State the blood parasite species.
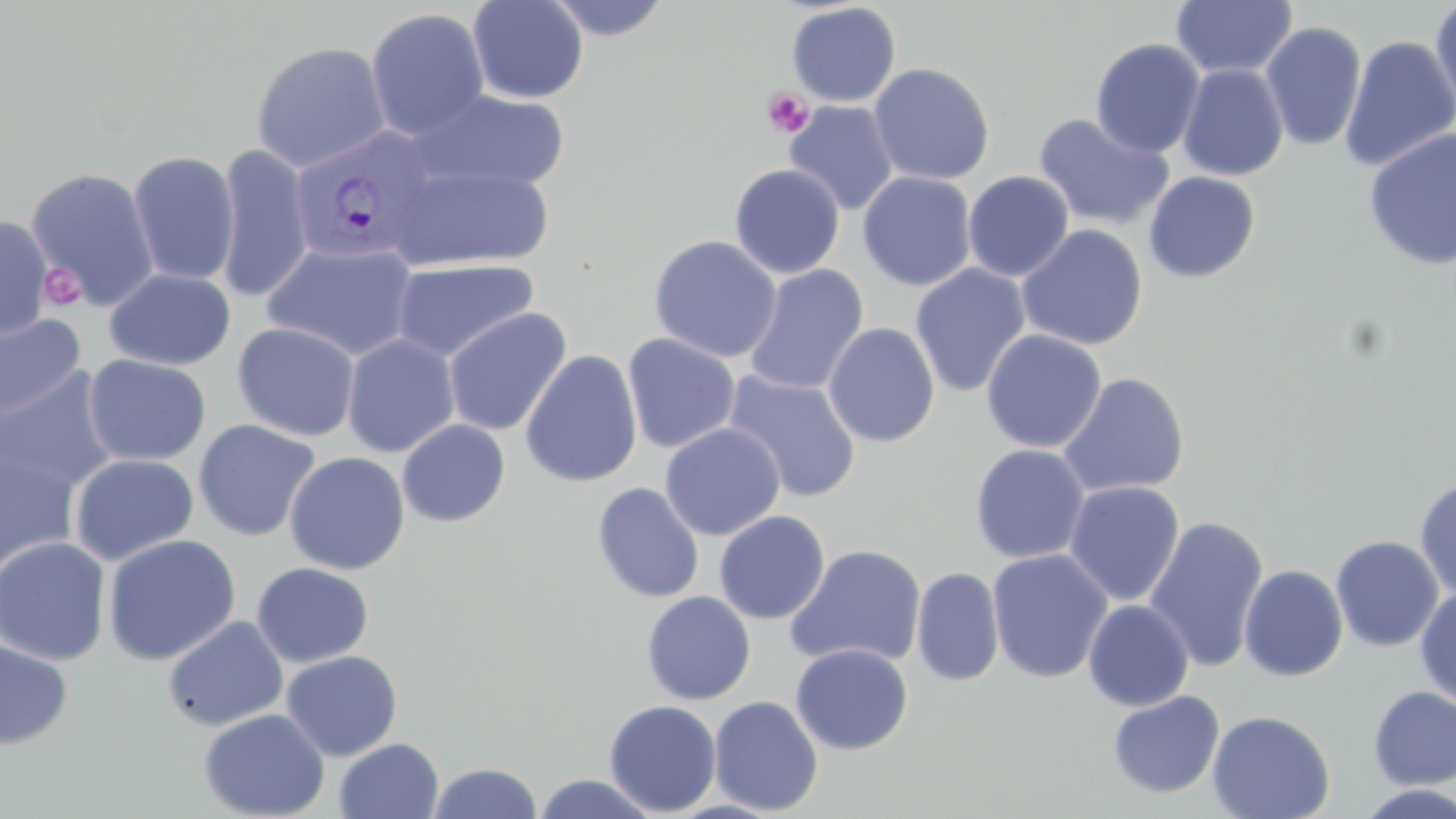

Plasmodium vivax.

image size = 1456×819 pixels
uninfected red blood cell locations = approximate bounding boxes as [x1, y1, x2, y2] in pixels: [467, 0, 588, 104], [543, 0, 673, 41], [1170, 0, 1298, 79], [1429, 0, 1456, 117], [785, 2, 902, 107], [365, 8, 490, 140], [1259, 21, 1367, 151], [1340, 35, 1456, 173], [1089, 38, 1205, 159], [251, 41, 391, 173], [867, 63, 994, 185], [1178, 64, 1289, 181], [408, 88, 570, 195], [784, 101, 900, 214], [1033, 113, 1174, 232], [1363, 127, 1456, 271], [215, 144, 313, 303], [128, 150, 240, 286], [387, 163, 555, 272], [729, 163, 845, 279], [25, 165, 160, 310], [963, 170, 1074, 281], [857, 171, 977, 291], [1143, 172, 1260, 283], [0, 214, 53, 339], [1016, 224, 1148, 350], [648, 235, 782, 363], [262, 241, 421, 363], [392, 259, 540, 363], [743, 264, 868, 396], [908, 264, 1031, 397], [104, 268, 235, 370], [442, 307, 572, 436], [0, 312, 86, 422], [232, 322, 360, 442], [823, 323, 940, 447], [981, 330, 1106, 453], [622, 332, 741, 454], [342, 333, 461, 457], [520, 349, 643, 488], [83, 354, 211, 467], [0, 366, 121, 495], [723, 371, 861, 504], [1057, 372, 1190, 497], [193, 419, 320, 542], [396, 419, 510, 527], [660, 423, 785, 541], [970, 443, 1090, 564], [0, 448, 81, 578], [284, 451, 410, 575], [69, 454, 199, 566], [1414, 475, 1456, 600], [1064, 480, 1185, 605], [591, 481, 705, 603], [714, 510, 830, 624], [1144, 516, 1269, 672], [102, 533, 241, 666], [1330, 534, 1444, 652], [0, 536, 111, 666], [784, 544, 927, 669], [987, 548, 1113, 683], [252, 563, 374, 667], [1238, 564, 1348, 681], [911, 567, 1005, 686], [1414, 586, 1456, 707], [641, 591, 756, 705], [1082, 599, 1195, 711], [162, 615, 288, 731], [0, 638, 73, 750], [790, 643, 913, 755], [280, 650, 403, 761], [1368, 686, 1456, 790], [1107, 690, 1225, 799], [709, 694, 824, 815], [603, 699, 722, 816], [199, 708, 331, 819], [1207, 710, 1335, 819], [333, 737, 444, 819], [427, 761, 544, 819], [530, 773, 663, 818]
preparation = thin blood smear
modality = optical microscopy
field of view = one of a larger specimen
platelet locations = approximate bounding boxes as [x1, y1, x2, y2] in pixels: [762, 88, 815, 138], [40, 263, 86, 312]
magnification = 1000x
stain = May-Grünwald-Giemsa
Plasmodium vivax-infected red blood cell locations = approximate bounding boxes as [x1, y1, x2, y2] in pixels: [288, 125, 437, 268]